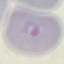
{
  "malaria_status": "parasitized",
  "capture": "smartphone through the microscope eyepiece",
  "preparation": "thin smear",
  "image_type": "automatically extracted cell patch, resized to 64 × 64 pixels",
  "stain": "Giemsa"
}